Name the cell type shown.
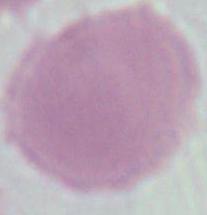

An erythrocyte.

Photomicrograph. 1000x magnification.